Assess the morphology of the erythrocytes.
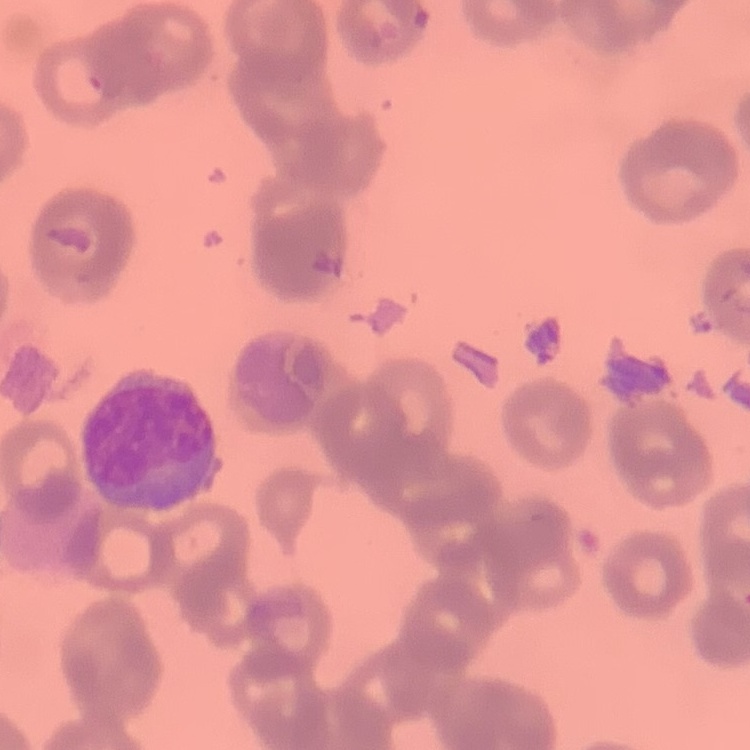
They show rouleaux formation.

{
  "image_type": "one tile cut from a larger photomicrograph",
  "preparation": "thin peripheral smear",
  "stain": "Field's or Giemsa"
}